Identify the parasite.
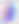
Toxoplasma gondii.

magnification: 400x
modality: photomicrograph